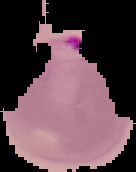
Summary:
  - Preparation: thin blood film
  - Image type: cell region segmented out of the field of view; surrounding area masked to black
  - Result: malaria parasites identified
  - Image size: 136×172 pixels